Assess this cell for malaria.
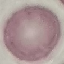
It is uninfected.

Thin blood film. Giemsa stain. Acquired by smartphone through the microscope eyepiece. Automatically extracted cell patch, resized to 64 × 64 pixels.